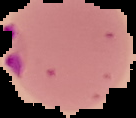
Image is 136×118 pixels. Malaria status: parasitized. Segmented cell region on a black background. From a thin blood smear.